Report the malaria status of this cell.
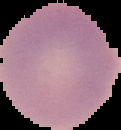

Uninfected.

Summary:
  - Image type: segmented cell region with the area outside set to black
  - Image size: 121×130 pixels
  - Preparation: thin blood smear